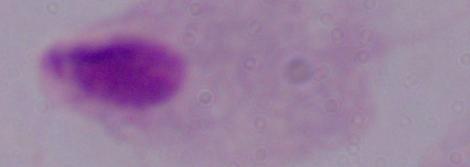
Captured at 1000x magnification. Micrograph. A trichomonad is shown.